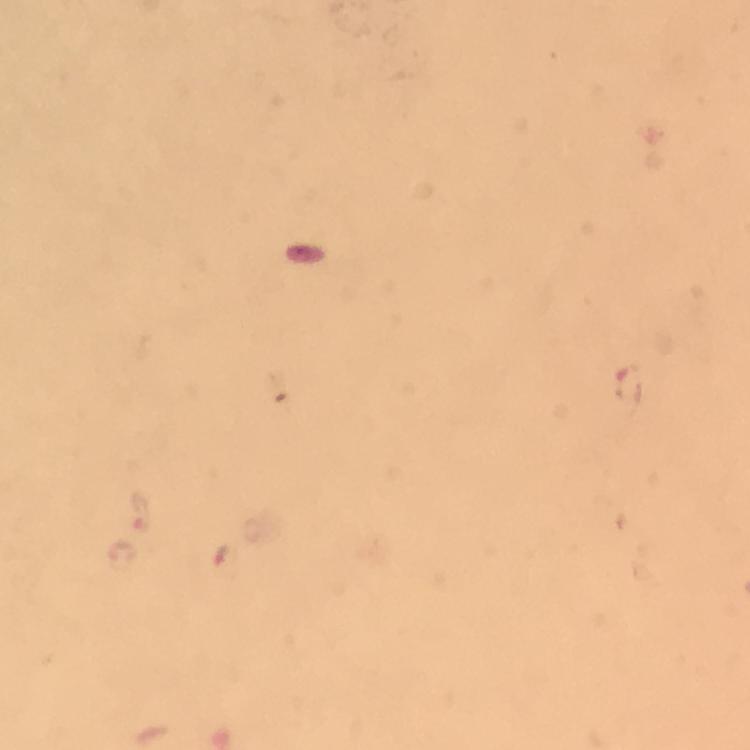
{
  "malaria_parasite_locations": "approximate centers as (x, y) in pixels: (628, 385), (142, 510), (225, 562)",
  "stain": "Giemsa",
  "immersion_oil": "applied",
  "image_size": "750×750 pixels",
  "context": "from a diagnostic examination for malaria",
  "preparation": "thick blood smear",
  "cropped_from": "a single field of view",
  "capture": "smartphone mounted on the microscope",
  "magnification": "100x"
}